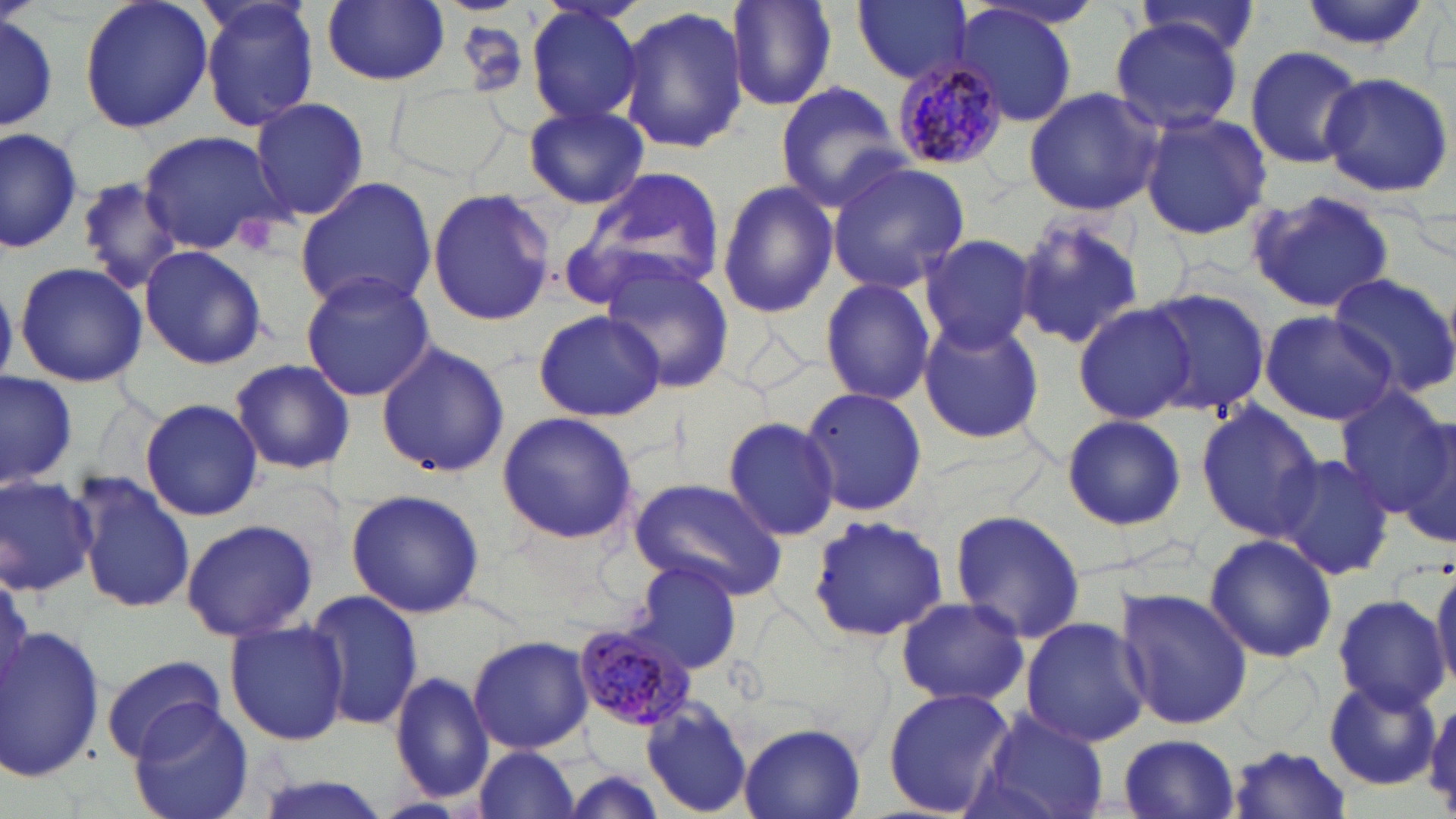
slide-level diagnosis = Plasmodium malariae
platelet locations = approximate bounding boxes as named x1/y1/x2/y2 corners in pixels: (x1=236, y1=214, x2=274, y2=255)
modality = light microscopy
stain = May-Grünwald-Giemsa
Plasmodium malariae-infected red blood cell locations = approximate bounding boxes as named x1/y1/x2/y2 corners in pixels: (x1=887, y1=57, x2=1008, y2=169), (x1=572, y1=620, x2=698, y2=733)
magnification = 1000x
image size = 1456×819 pixels
uninfected red blood cell locations = approximate bounding boxes as named x1/y1/x2/y2 corners in pixels: (x1=77, y1=0, x2=214, y2=135), (x1=194, y1=0, x2=323, y2=133), (x1=727, y1=0, x2=839, y2=112), (x1=853, y1=0, x2=973, y2=86), (x1=1296, y1=0, x2=1431, y2=53), (x1=320, y1=1, x2=450, y2=86), (x1=523, y1=2, x2=648, y2=130), (x1=1128, y1=4, x2=1266, y2=67), (x1=0, y1=5, x2=62, y2=137), (x1=617, y1=5, x2=746, y2=156), (x1=953, y1=5, x2=1079, y2=128), (x1=1108, y1=19, x2=1243, y2=134), (x1=1244, y1=45, x2=1363, y2=170), (x1=1318, y1=71, x2=1454, y2=198), (x1=775, y1=81, x2=906, y2=210), (x1=394, y1=83, x2=504, y2=177), (x1=1022, y1=87, x2=1167, y2=215), (x1=251, y1=97, x2=369, y2=220), (x1=520, y1=103, x2=652, y2=207), (x1=1138, y1=113, x2=1272, y2=240), (x1=0, y1=125, x2=81, y2=252), (x1=137, y1=129, x2=285, y2=257), (x1=827, y1=160, x2=971, y2=293), (x1=573, y1=167, x2=727, y2=300), (x1=76, y1=175, x2=185, y2=294), (x1=294, y1=175, x2=438, y2=313), (x1=714, y1=177, x2=840, y2=320), (x1=1245, y1=187, x2=1397, y2=313), (x1=425, y1=188, x2=557, y2=326), (x1=1015, y1=211, x2=1145, y2=352), (x1=916, y1=234, x2=1035, y2=354), (x1=139, y1=244, x2=267, y2=371), (x1=592, y1=255, x2=736, y2=396), (x1=14, y1=262, x2=149, y2=389), (x1=298, y1=269, x2=438, y2=401), (x1=1324, y1=271, x2=1456, y2=397), (x1=819, y1=276, x2=936, y2=406), (x1=1139, y1=286, x2=1272, y2=420), (x1=1077, y1=304, x2=1198, y2=423), (x1=533, y1=309, x2=665, y2=421), (x1=1258, y1=310, x2=1398, y2=426), (x1=915, y1=317, x2=1045, y2=445), (x1=376, y1=341, x2=510, y2=480), (x1=228, y1=358, x2=357, y2=475), (x1=0, y1=370, x2=78, y2=491), (x1=800, y1=385, x2=926, y2=519), (x1=1336, y1=391, x2=1456, y2=516), (x1=140, y1=396, x2=263, y2=522), (x1=1195, y1=403, x2=1323, y2=542), (x1=495, y1=412, x2=639, y2=544), (x1=1061, y1=412, x2=1189, y2=532), (x1=722, y1=416, x2=841, y2=540), (x1=1397, y1=420, x2=1456, y2=551), (x1=1271, y1=453, x2=1397, y2=580), (x1=0, y1=473, x2=99, y2=597), (x1=74, y1=473, x2=194, y2=615), (x1=629, y1=478, x2=787, y2=599), (x1=343, y1=488, x2=485, y2=617), (x1=949, y1=509, x2=1086, y2=645), (x1=805, y1=514, x2=950, y2=643), (x1=181, y1=518, x2=317, y2=642), (x1=1203, y1=533, x2=1338, y2=664), (x1=632, y1=559, x2=744, y2=673), (x1=1428, y1=564, x2=1456, y2=698), (x1=1115, y1=588, x2=1252, y2=730), (x1=303, y1=590, x2=424, y2=733), (x1=1332, y1=594, x2=1449, y2=714), (x1=894, y1=597, x2=1028, y2=708), (x1=226, y1=617, x2=347, y2=747), (x1=1021, y1=617, x2=1150, y2=748), (x1=1, y1=624, x2=104, y2=783), (x1=468, y1=634, x2=593, y2=754), (x1=100, y1=655, x2=228, y2=760), (x1=391, y1=671, x2=497, y2=804), (x1=1322, y1=679, x2=1440, y2=790), (x1=882, y1=687, x2=1018, y2=818), (x1=1424, y1=697, x2=1456, y2=806), (x1=640, y1=698, x2=756, y2=816), (x1=129, y1=701, x2=255, y2=819), (x1=974, y1=708, x2=1109, y2=819), (x1=738, y1=723, x2=867, y2=818), (x1=1115, y1=734, x2=1242, y2=818), (x1=1227, y1=743, x2=1352, y2=817), (x1=470, y1=745, x2=582, y2=819), (x1=550, y1=765, x2=673, y2=819), (x1=247, y1=772, x2=390, y2=819), (x1=372, y1=794, x2=474, y2=819)
field of view = one of a larger specimen
preparation = thin blood smear